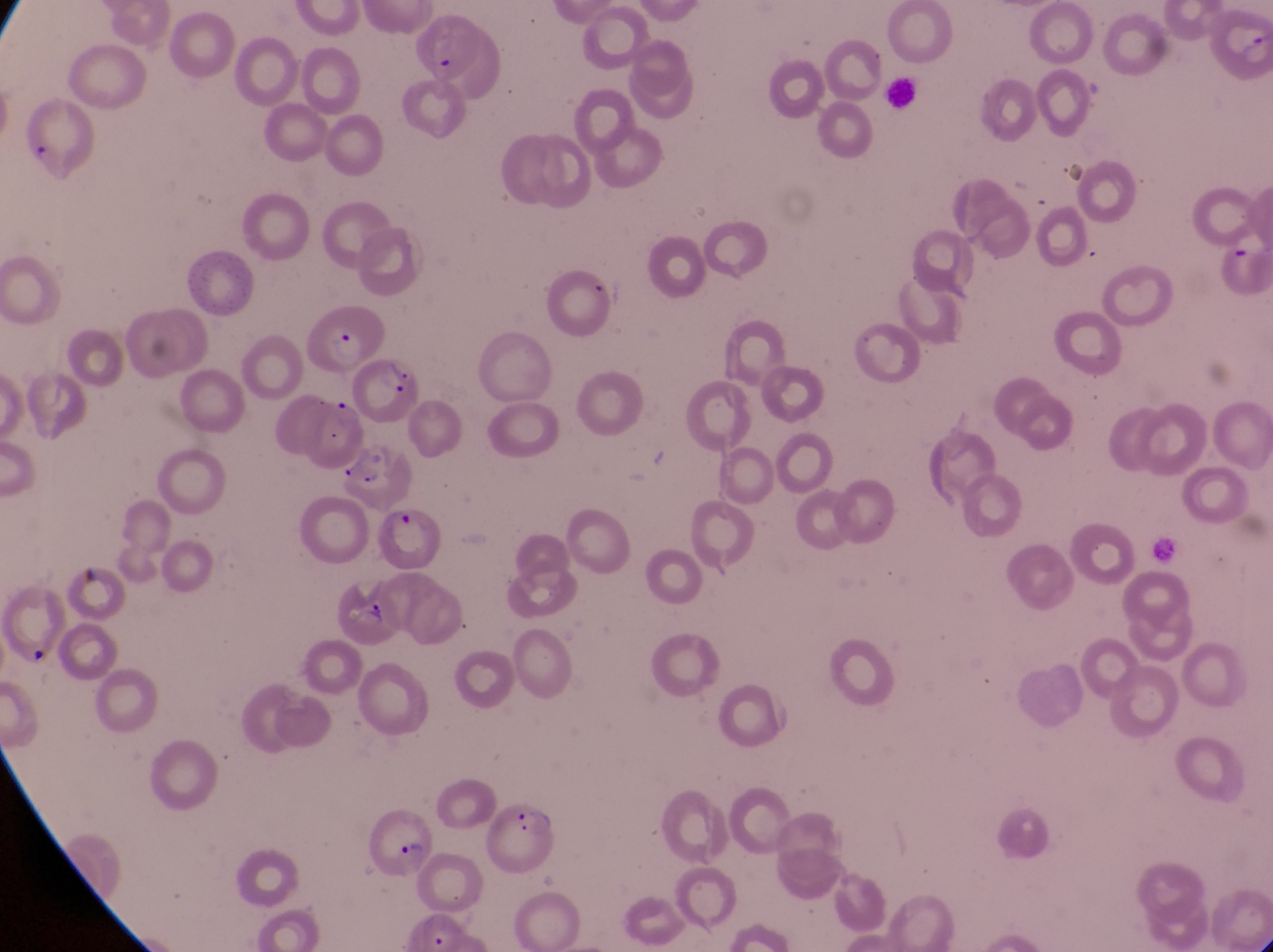

artifact (platelet-like body, stain precipitate, or debris) locations = approximate bounding boxes as left top right bottom in pixels: 75 554 105 591; 27 637 49 662
capture = smartphone photograph through the eyepiece of an Olympus CX-23 microscope
parasitised red blood cell locations = approximate bounding boxes as left top right bottom in pixels: 312 299 384 364; 349 354 416 424; 345 440 419 507; 357 504 447 572; 334 572 401 649; 482 794 567 876; 369 809 443 881
country = Uganda
magnification = 1000x
leukocyte locations = approximate bounding boxes as left top right bottom in pixels: 886 75 920 108
field of view = single
preparation = thin blood film
image size = 1273×952 pixels